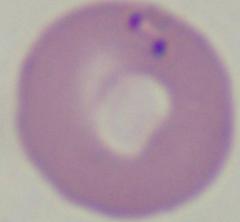

Summary:
  - Modality: micrograph
  - Identification: Babesia
  - Magnification: 1000x